Locate and identify every blood parasite.
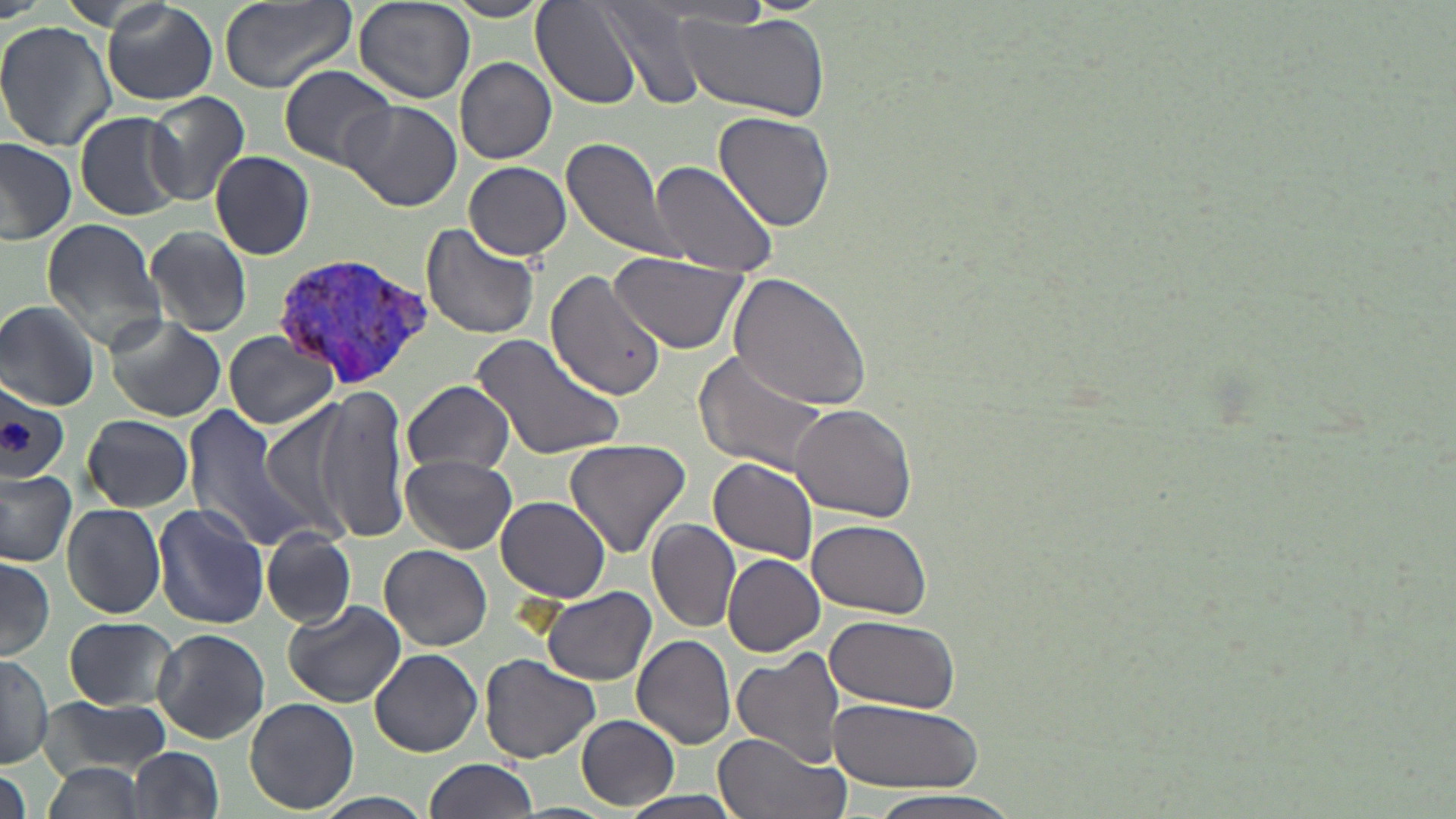
Approximate bounding boxes as (x1, y1, x2, y2) in pixels.
Plasmodium vivax-infected red blood cells: (276, 250, 435, 394).
No Plasmodium falciparum, Plasmodium ovale, Plasmodium malariae, Babesia divergens, or Trypanosoma brucei observed.

slide_level_diagnosis: Plasmodium vivax
modality: light microscopy
uninfected_red_blood_cell_locations: 'approximate bounding boxes as (x1, y1, x2, y2) in pixels: (219, 0, 358, 97), (351, 0, 475, 104), (102, 1, 218, 106), (439, 1, 554, 21), (535, 2, 647, 110), (597, 5, 711, 112), (678, 13, 830, 123), (0, 23, 115, 150), (454, 56, 555, 164), (278, 65, 399, 169), (145, 91, 250, 204), (339, 98, 463, 211), (712, 110, 837, 234), (75, 111, 188, 220), (560, 136, 682, 264), (0, 138, 77, 248), (209, 150, 315, 260), (649, 161, 780, 277), (463, 162, 571, 260), (41, 218, 167, 352), (422, 224, 541, 342), (146, 225, 252, 335), (606, 251, 752, 356), (545, 268, 667, 402), (728, 273, 872, 412), (0, 300, 100, 409), (105, 316, 226, 422), (224, 330, 340, 430), (470, 333, 626, 462), (696, 351, 835, 476), (403, 380, 515, 476), (0, 381, 71, 483), (315, 387, 411, 544), (257, 398, 367, 537), (789, 403, 917, 522), (181, 405, 308, 547), (82, 415, 194, 511), (563, 437, 693, 559), (401, 455, 516, 553), (709, 458, 820, 562), (0, 470, 77, 567), (495, 495, 612, 603), (61, 502, 167, 620), (151, 503, 268, 629), (808, 518, 932, 619), (648, 519, 741, 631), (261, 528, 357, 627), (642, 534, 822, 641), (378, 544, 492, 652), (0, 553, 56, 661), (722, 553, 825, 657), (539, 584, 654, 685), (282, 601, 405, 707), (826, 615, 961, 713), (65, 618, 181, 711), (151, 628, 270, 744), (632, 633, 737, 749), (369, 649, 483, 758), (732, 649, 846, 768), (480, 653, 600, 763), (1, 656, 53, 767), (39, 694, 174, 777), (244, 697, 358, 815), (828, 700, 985, 793), (577, 715, 678, 811), (714, 732, 846, 819), (129, 747, 226, 819), (426, 757, 539, 818), (36, 763, 150, 819), (1, 766, 29, 819), (619, 790, 748, 819), (862, 790, 1020, 818), (316, 792, 436, 819)'
preparation: thin blood film
image_size: 1456×819 pixels
magnification: 1000x
stain: May-Grünwald-Giemsa
platelet_locations: 'approximate bounding boxes as (x1, y1, x2, y2) in pixels: (0, 421, 35, 453)'
field_of_view: single